Describe the morphology of the red blood cells.
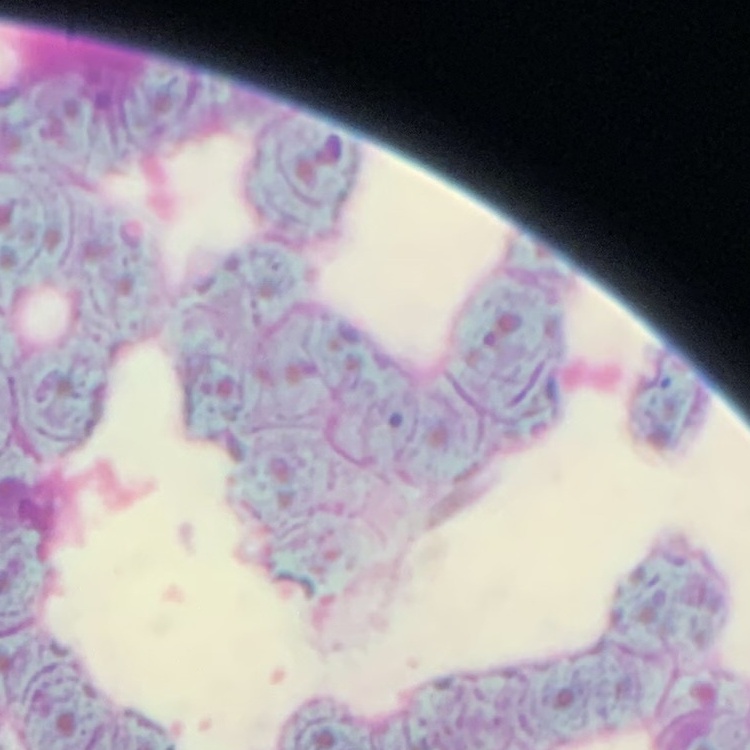
They show rouleaux formation.

image_type: square crop of a larger photomicrograph
preparation: thin peripheral smear
stain: Field's or Giemsa